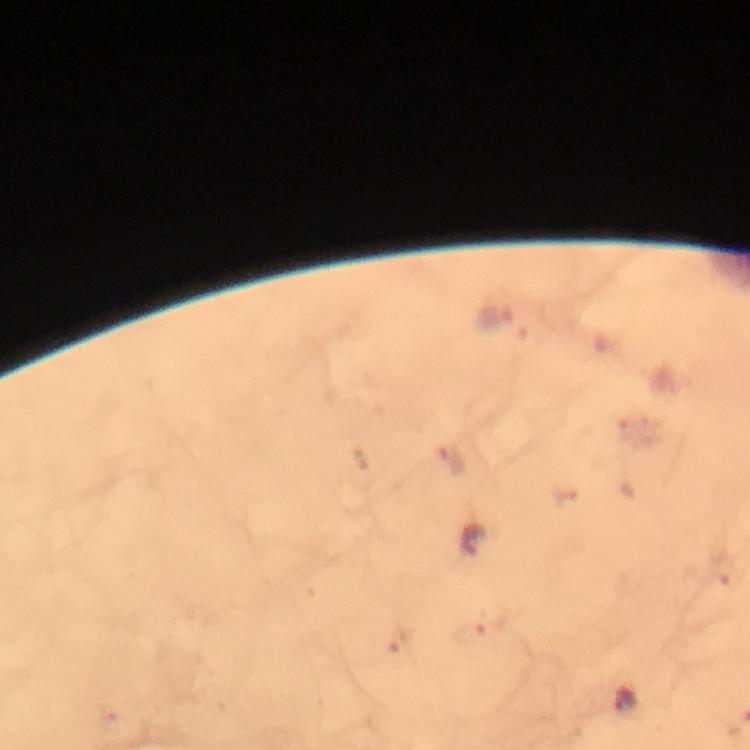

{
  "image_size": "750×750 pixels",
  "magnification": "100x",
  "capture": "smartphone photograph through a microscope",
  "immersion_oil": "applied",
  "context": "from a malaria diagnostic workup",
  "cropped_from": "a single field of view",
  "plasmodium_parasite_locations": "approximate object centers, in pixels from the top-left corner: (x=496, y=316), (x=449, y=460), (x=726, y=570), (x=472, y=637), (x=397, y=646), (x=623, y=703)",
  "preparation": "thick smear",
  "stain": "Giemsa"
}